Assess the morphology of the erythrocytes.
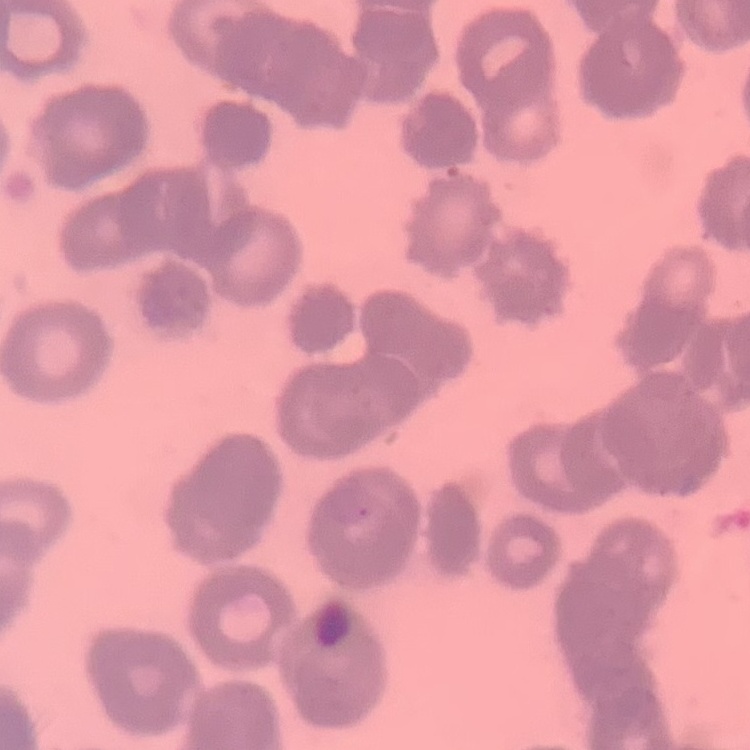
They show rouleaux formation.

image type = square crop of a larger photomicrograph
preparation = thin peripheral smear
stain = Field's or Giemsa